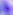 Toxoplasma gondii is shown. Photomicrograph. Captured at 400x magnification.